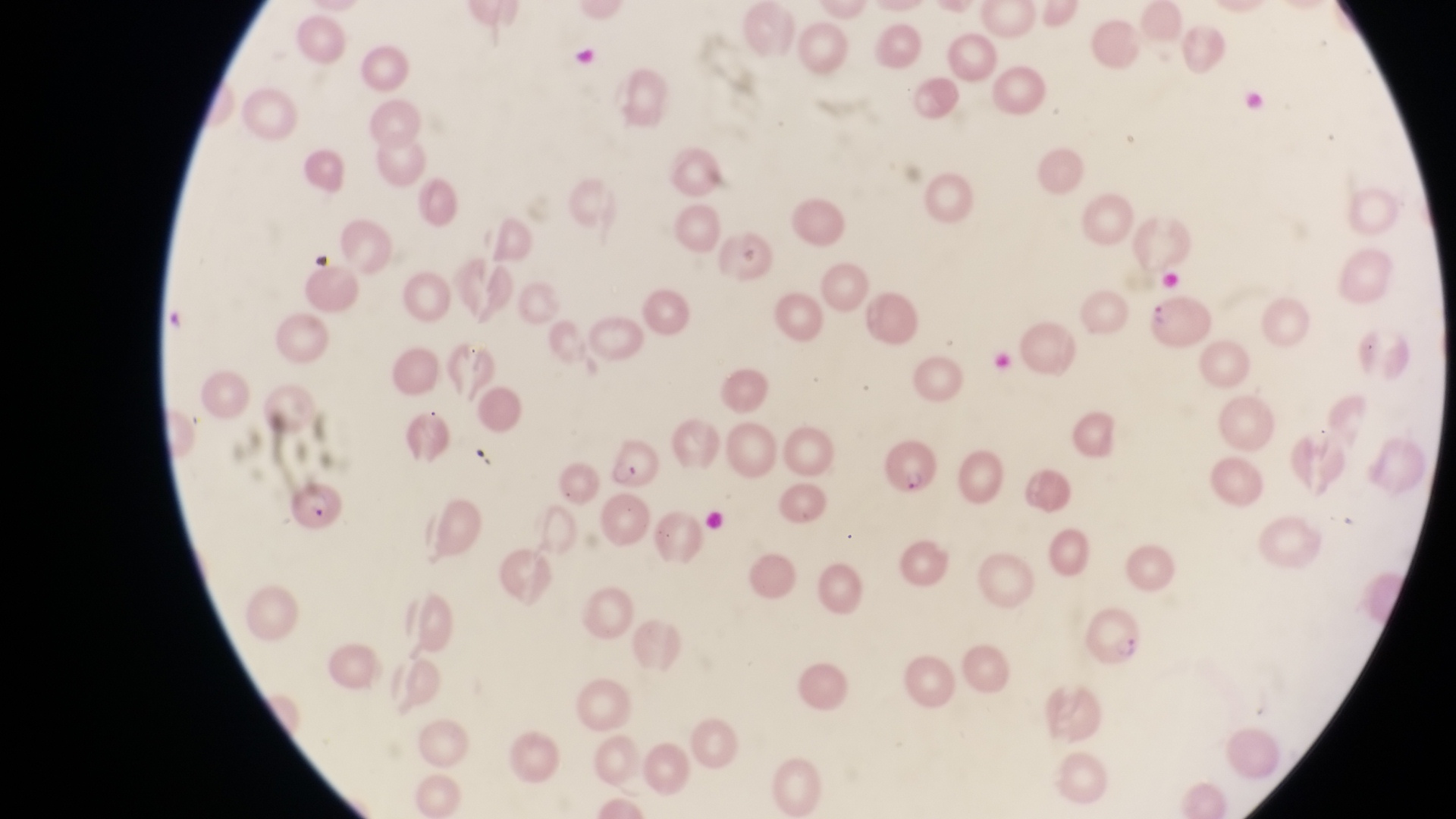 Approximate bounding boxes as left top right bottom in pixels. Parasitised red blood cell locations: 1150 291 1214 354; 888 433 940 496; 605 436 658 495; 284 481 348 537; 1089 605 1148 676. Collected in Uganda. Photographed through the eyepiece of an Olympus CX-23 microscope with a smartphone camera. Thin blood smear. Image is 1456×819 pixels. One field of view. At a magnification of 1000x.